Identify the blood parasite species.
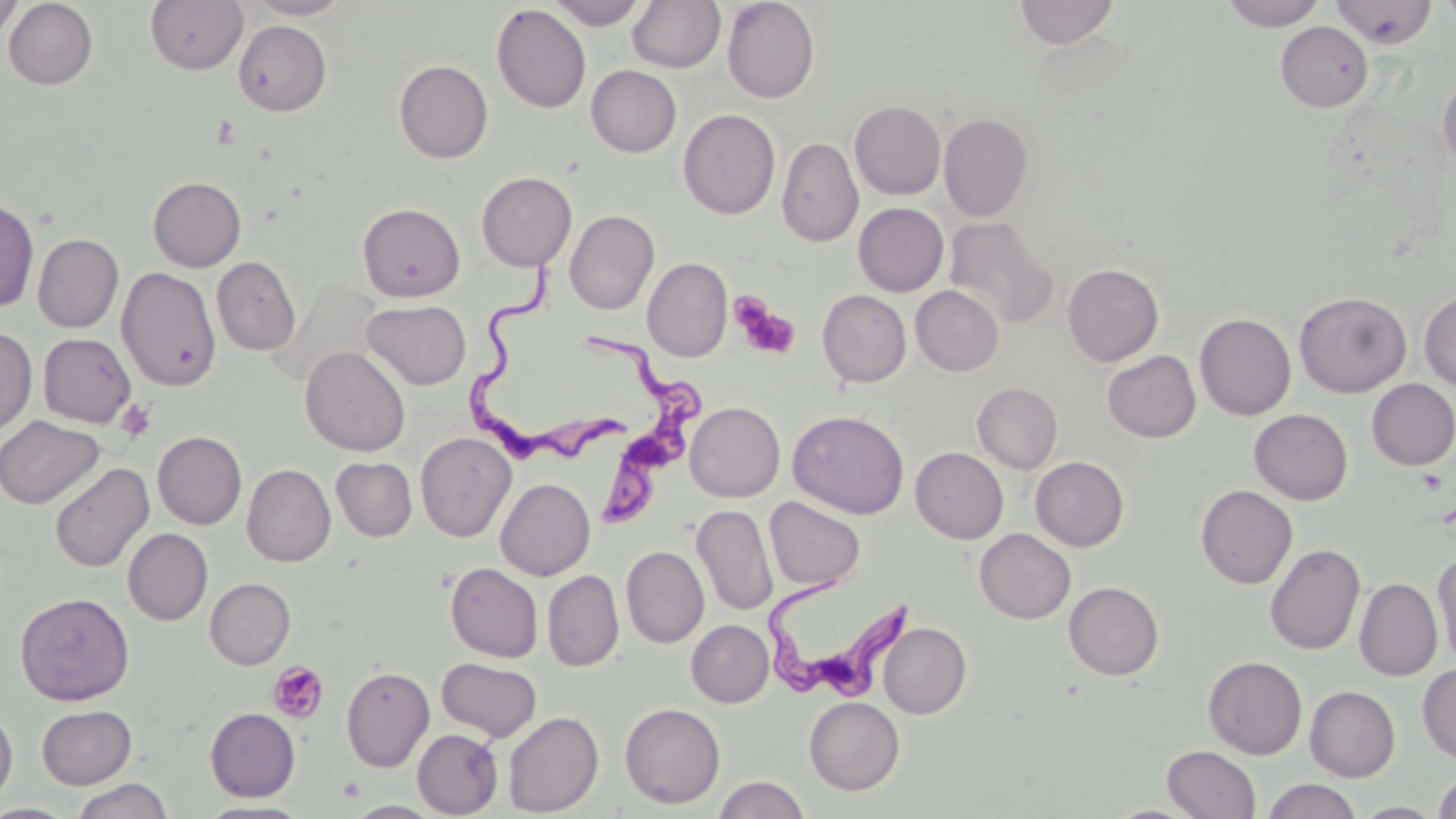
Trypanosoma brucei.

Summary:
  - Coordinate format: approximate bounding boxes as named x1/y1/x2/y2 corners in pixels
  - Platelet locations: (x1=732, y1=297, x2=800, y2=359), (x1=115, y1=399, x2=156, y2=442), (x1=267, y1=661, x2=329, y2=723)
  - Trypanosoma brucei locations: (x1=471, y1=246, x2=638, y2=469), (x1=580, y1=329, x2=711, y2=522), (x1=764, y1=579, x2=913, y2=702)
  - Uninfected red blood cell locations: (x1=0, y1=0, x2=22, y2=47), (x1=3, y1=0, x2=99, y2=89), (x1=145, y1=0, x2=248, y2=75), (x1=245, y1=0, x2=353, y2=20), (x1=547, y1=0, x2=649, y2=29), (x1=721, y1=0, x2=820, y2=103), (x1=1014, y1=0, x2=1119, y2=49), (x1=1220, y1=0, x2=1326, y2=30), (x1=627, y1=1, x2=725, y2=73), (x1=1332, y1=1, x2=1436, y2=48), (x1=1439, y1=1, x2=1456, y2=26), (x1=491, y1=4, x2=591, y2=113), (x1=233, y1=20, x2=331, y2=116), (x1=1276, y1=22, x2=1372, y2=112), (x1=394, y1=60, x2=493, y2=163), (x1=586, y1=65, x2=681, y2=157), (x1=1437, y1=72, x2=1456, y2=169), (x1=850, y1=100, x2=946, y2=199), (x1=678, y1=109, x2=780, y2=219), (x1=939, y1=112, x2=1034, y2=222), (x1=777, y1=137, x2=863, y2=247), (x1=476, y1=172, x2=577, y2=272), (x1=147, y1=176, x2=246, y2=271), (x1=0, y1=196, x2=39, y2=313), (x1=357, y1=202, x2=466, y2=302), (x1=854, y1=203, x2=949, y2=296), (x1=564, y1=209, x2=659, y2=315), (x1=943, y1=217, x2=1058, y2=329), (x1=32, y1=233, x2=124, y2=333), (x1=211, y1=256, x2=301, y2=356), (x1=642, y1=257, x2=732, y2=362), (x1=1062, y1=263, x2=1164, y2=366), (x1=116, y1=267, x2=221, y2=391), (x1=911, y1=285, x2=1003, y2=376), (x1=817, y1=289, x2=912, y2=387), (x1=1294, y1=291, x2=1411, y2=397), (x1=1419, y1=291, x2=1456, y2=391), (x1=362, y1=300, x2=471, y2=390), (x1=1195, y1=313, x2=1296, y2=421), (x1=0, y1=326, x2=37, y2=438), (x1=38, y1=333, x2=136, y2=427), (x1=300, y1=345, x2=411, y2=457), (x1=1102, y1=350, x2=1200, y2=442), (x1=1367, y1=379, x2=1456, y2=470), (x1=973, y1=383, x2=1062, y2=473), (x1=684, y1=402, x2=785, y2=502), (x1=1249, y1=408, x2=1353, y2=505), (x1=787, y1=410, x2=909, y2=519), (x1=0, y1=416, x2=104, y2=509), (x1=153, y1=431, x2=247, y2=529), (x1=416, y1=432, x2=516, y2=541), (x1=910, y1=447, x2=1008, y2=544), (x1=1030, y1=456, x2=1128, y2=551), (x1=331, y1=457, x2=417, y2=541), (x1=49, y1=462, x2=153, y2=574), (x1=242, y1=464, x2=336, y2=566), (x1=495, y1=478, x2=595, y2=580), (x1=1196, y1=485, x2=1297, y2=589), (x1=764, y1=497, x2=865, y2=593), (x1=691, y1=505, x2=777, y2=616), (x1=122, y1=528, x2=213, y2=625), (x1=975, y1=529, x2=1075, y2=623), (x1=1265, y1=543, x2=1365, y2=655), (x1=621, y1=545, x2=709, y2=648), (x1=1432, y1=547, x2=1456, y2=667), (x1=445, y1=563, x2=543, y2=662), (x1=543, y1=570, x2=624, y2=671), (x1=205, y1=578, x2=295, y2=669), (x1=1355, y1=578, x2=1443, y2=681), (x1=1063, y1=581, x2=1164, y2=680), (x1=15, y1=592, x2=135, y2=706), (x1=686, y1=619, x2=773, y2=707), (x1=879, y1=622, x2=971, y2=719), (x1=1203, y1=656, x2=1307, y2=759), (x1=437, y1=657, x2=542, y2=742), (x1=1417, y1=664, x2=1456, y2=762), (x1=341, y1=666, x2=435, y2=771), (x1=1305, y1=686, x2=1400, y2=782), (x1=804, y1=696, x2=905, y2=795), (x1=0, y1=702, x2=18, y2=807), (x1=619, y1=702, x2=726, y2=808), (x1=36, y1=705, x2=136, y2=789), (x1=205, y1=707, x2=300, y2=801), (x1=504, y1=710, x2=724, y2=811), (x1=503, y1=711, x2=603, y2=816), (x1=412, y1=728, x2=503, y2=817), (x1=1162, y1=745, x2=1261, y2=819), (x1=1433, y1=770, x2=1456, y2=819), (x1=714, y1=775, x2=810, y2=819), (x1=70, y1=778, x2=173, y2=819), (x1=1263, y1=778, x2=1362, y2=819), (x1=196, y1=800, x2=313, y2=818), (x1=344, y1=800, x2=443, y2=817), (x1=0, y1=803, x2=78, y2=818)
  - Magnification: 1000x
  - Modality: optical microscopy
  - Image size: 1456×819 pixels
  - Stain: May-Grünwald-Giemsa
  - Field of view: single
  - Preparation: thin blood film